Assess this cell for malaria.
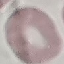
Uninfected.

Cell patch, automatically extracted from a larger field of view and resized to 64 × 64 pixels. Thin smear of blood. Acquired by smartphone through the microscope eyepiece. Giemsa-stained preparation.